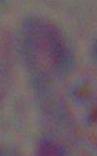

Toxoplasma gondii is shown. Captured at 1000x magnification. Photomicrograph.